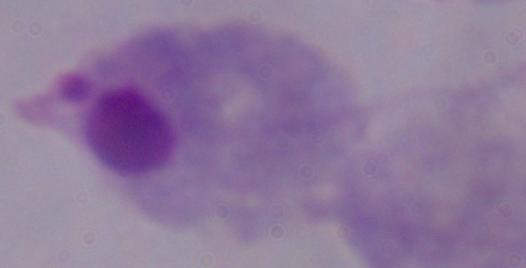
Summary:
  - Magnification: 1000x
  - Modality: photomicrograph
  - Identification: trichomonad